Give the position of every Plasmodium parasite.
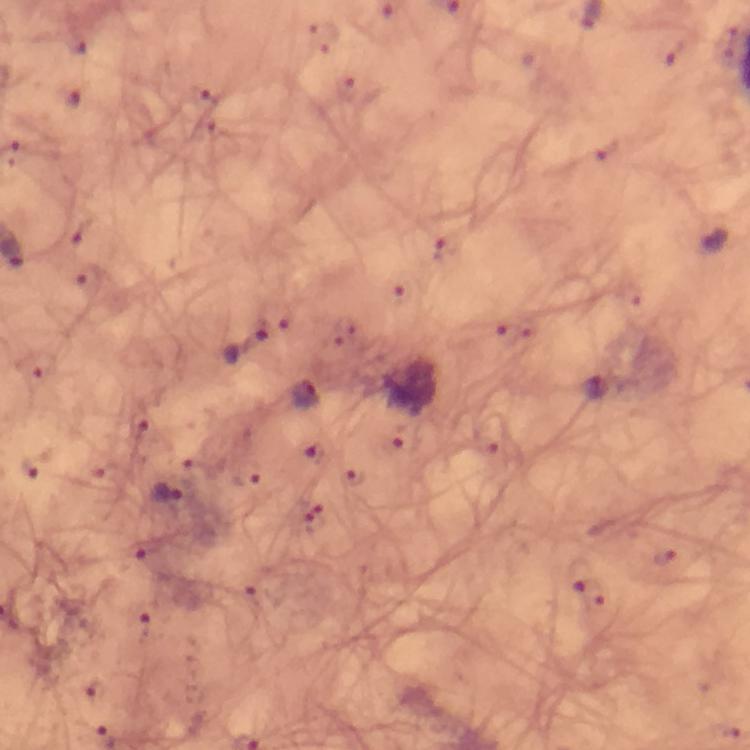

Approximate object centers, in pixels from the top-left corner.
Plasmodium parasites: (x=77, y=46), (x=676, y=54), (x=206, y=96), (x=72, y=97), (x=607, y=151), (x=81, y=232), (x=445, y=247), (x=90, y=279), (x=400, y=295), (x=506, y=334), (x=244, y=344), (x=35, y=366), (x=304, y=394), (x=140, y=440), (x=315, y=453), (x=31, y=470), (x=356, y=480), (x=169, y=490), (x=143, y=550), (x=578, y=575).

stain = Giemsa
capture = smartphone photograph through a microscope
image size = 750×750 pixels
context = from a diagnostic examination for malaria
immersion oil = used
preparation = thick blood smear
magnification = 100x
cropped from = a single field of view